Report the malaria status of this cell.
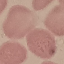

It is uninfected.

Summary:
  - Image type: cell patch, automatically extracted from a larger field of view and resized to 64 × 64 pixels
  - Capture: smartphone through the microscope eyepiece
  - Preparation: thin smear
  - Stain: Giemsa